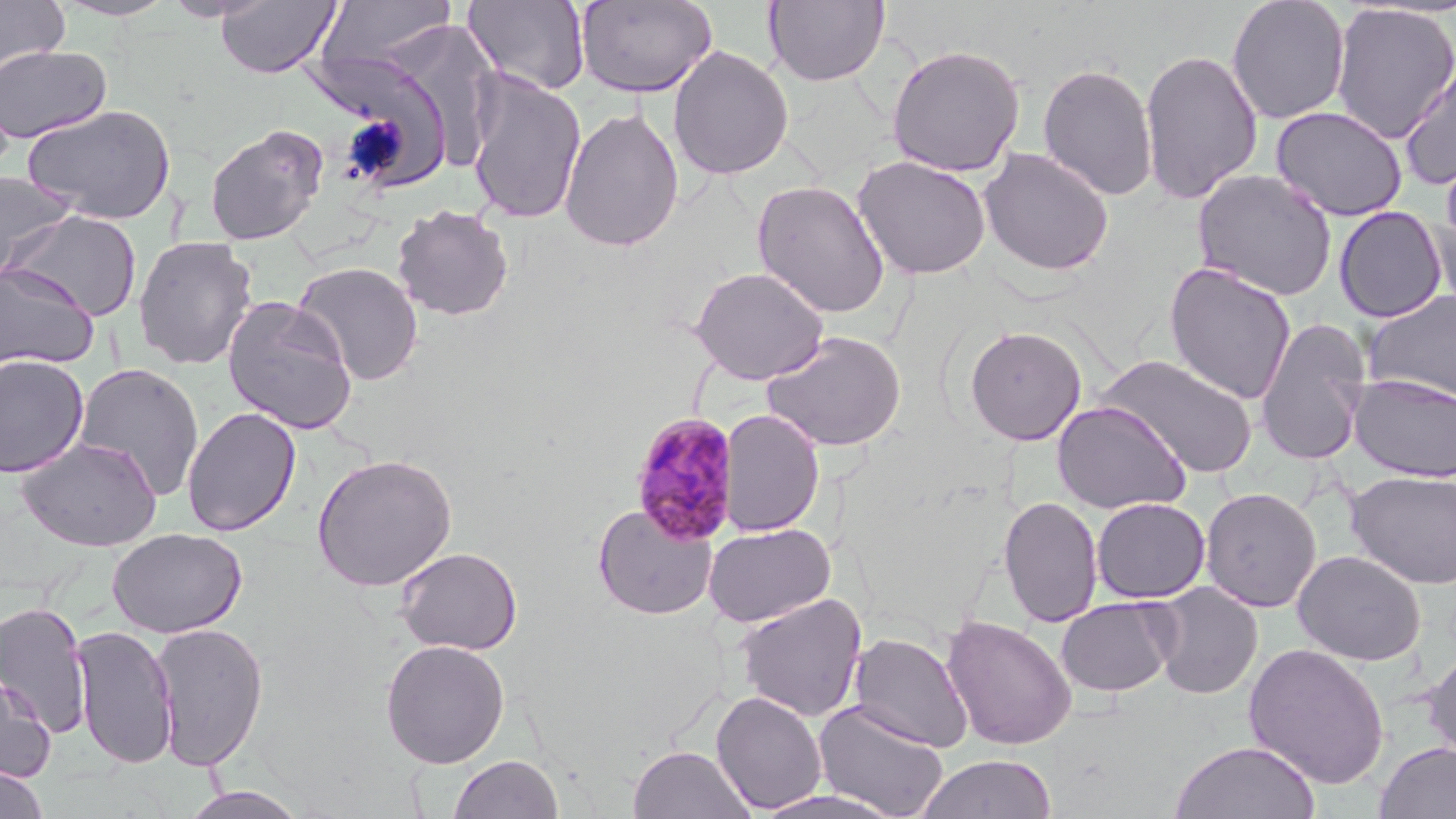

{
  "slide_level_diagnosis": "Plasmodium malariae",
  "magnification": "1000x",
  "stain": "May-Grünwald-Giemsa",
  "image_size": "1456×819 pixels",
  "uninfected_red_blood_cell_locations": "approximate bounding boxes as [x1, y1, x2, y2] in pixels: [0, 0, 70, 76], [50, 0, 181, 21], [163, 0, 271, 22], [215, 0, 341, 78], [575, 0, 717, 98], [1226, 0, 1350, 124], [315, 1, 460, 75], [463, 1, 590, 96], [763, 1, 890, 86], [1330, 3, 1456, 144], [350, 31, 498, 181], [886, 43, 1025, 177], [0, 45, 111, 144], [668, 46, 794, 181], [1139, 48, 1263, 205], [1399, 58, 1456, 190], [1037, 62, 1159, 201], [465, 70, 587, 225], [323, 77, 439, 187], [22, 103, 177, 225], [559, 105, 685, 254], [1271, 105, 1408, 221], [204, 123, 329, 246], [979, 147, 1114, 276], [1441, 147, 1456, 255], [853, 155, 992, 279], [1191, 168, 1338, 301], [0, 171, 76, 280], [752, 180, 891, 319], [1422, 196, 1456, 312], [391, 204, 514, 321], [1334, 206, 1448, 323], [5, 209, 143, 322], [132, 236, 258, 371], [291, 260, 424, 386], [1163, 262, 1297, 405], [0, 263, 100, 372], [688, 266, 830, 385], [1362, 290, 1456, 404], [221, 296, 358, 435], [1255, 317, 1372, 465], [964, 324, 1088, 446], [761, 330, 907, 452], [0, 354, 90, 478], [1096, 354, 1259, 478], [72, 362, 206, 501], [1349, 374, 1456, 483], [1052, 400, 1191, 515], [182, 406, 301, 537], [719, 408, 825, 538], [15, 436, 164, 551], [311, 453, 458, 592], [1346, 470, 1456, 589], [1200, 487, 1322, 613], [998, 495, 1104, 628], [1091, 497, 1210, 603], [592, 502, 718, 620], [703, 522, 836, 628], [108, 527, 247, 638], [394, 546, 522, 655], [1293, 550, 1426, 666], [1150, 582, 1263, 700], [734, 593, 868, 722], [1056, 596, 1176, 697], [0, 600, 93, 738], [941, 614, 1077, 751], [150, 622, 269, 771], [71, 624, 178, 770], [847, 632, 974, 753], [380, 639, 510, 768], [1242, 643, 1391, 789], [1421, 647, 1456, 771], [0, 673, 56, 785], [711, 690, 828, 814], [813, 699, 950, 819], [1168, 740, 1320, 819], [1374, 742, 1456, 819], [628, 745, 756, 819], [917, 753, 1057, 819], [447, 754, 564, 818], [0, 766, 50, 819], [179, 786, 308, 819], [751, 788, 905, 818]",
  "preparation": "thin blood smear",
  "modality": "optical microscopy",
  "plasmodium_malariae_infected_red_blood_cell_locations": "approximate bounding boxes as [x1, y1, x2, y2] in pixels: [629, 411, 742, 547]",
  "field_of_view": "one of a larger specimen"
}